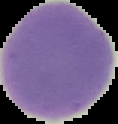

Summary:
  - Result: no Plasmodium parasites detected
  - Image size: 118×124 pixels
  - Image type: cell region segmented out of the field of view; surrounding area masked to black
  - Preparation: thin blood film